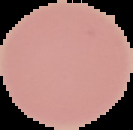

preparation: thin blood film
image_type: cell region segmented out of the field of view; surrounding area masked to black
image_size: 133×130 pixels
malaria_status: uninfected